Name the blood parasite species.
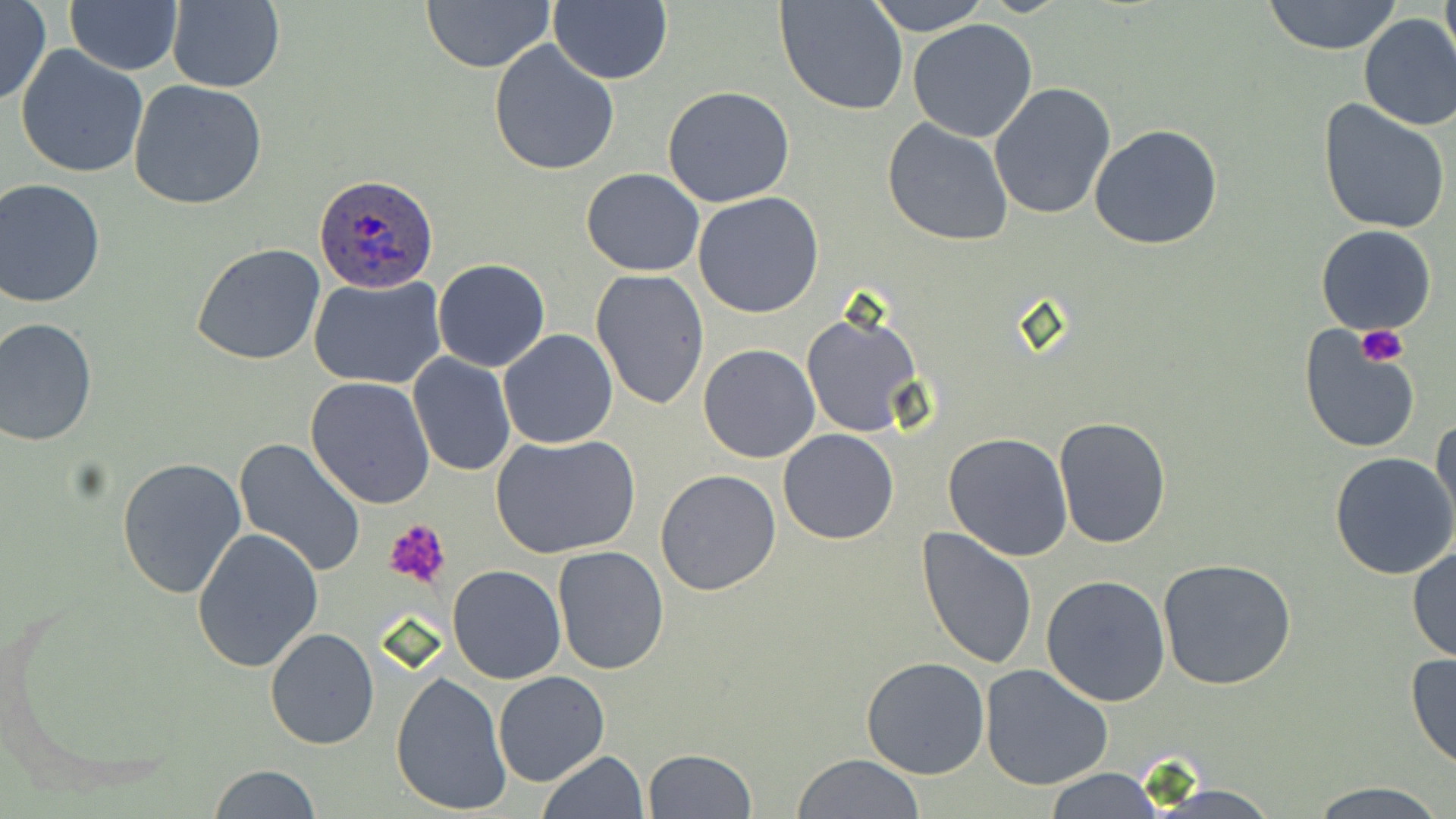

Plasmodium ovale.

Approximate bounding boxes as (x1, y1, x2, y2) in pixels. Uninfected red blood cell locations: (549, 0, 671, 84), (776, 0, 909, 117), (867, 0, 990, 35), (1263, 0, 1404, 55), (1439, 0, 1455, 71), (67, 1, 181, 75), (422, 1, 555, 73), (0, 2, 49, 106), (166, 2, 285, 92), (1357, 13, 1456, 131), (907, 18, 1039, 142), (489, 40, 620, 175), (15, 44, 149, 178), (128, 80, 268, 210), (987, 82, 1116, 220), (662, 86, 796, 209), (1317, 98, 1452, 235), (882, 118, 1014, 247), (1088, 123, 1223, 250), (581, 168, 704, 276), (0, 178, 106, 308), (692, 192, 824, 319), (1316, 224, 1438, 335), (191, 242, 327, 366), (432, 258, 550, 372), (590, 269, 710, 412), (307, 276, 447, 388), (801, 308, 924, 438), (0, 318, 97, 446), (1298, 325, 1421, 451), (497, 330, 618, 448), (699, 344, 819, 463), (407, 352, 516, 476), (305, 375, 437, 508), (1053, 417, 1171, 548), (1430, 418, 1456, 538), (777, 428, 900, 545), (942, 431, 1074, 561), (490, 432, 641, 560), (233, 439, 368, 578), (1330, 450, 1456, 579), (115, 455, 247, 600), (655, 468, 782, 595), (191, 526, 325, 673), (915, 527, 1037, 671), (1408, 545, 1456, 664), (552, 546, 670, 677), (1157, 557, 1298, 690), (444, 565, 566, 685), (1040, 573, 1171, 707), (265, 627, 380, 751), (1405, 651, 1456, 770), (862, 656, 989, 779), (979, 664, 1114, 790), (390, 671, 511, 816), (493, 671, 610, 788), (643, 748, 759, 818), (537, 750, 649, 819), (794, 752, 924, 819), (208, 764, 322, 818), (1040, 767, 1165, 819), (1303, 779, 1448, 817). Plasmodium ovale-infected red blood cell locations: (314, 175, 440, 294). Platelet locations: (1356, 326, 1407, 367), (385, 518, 453, 590). May-Grünwald-Giemsa stain. Image is 1456×819 pixels. Thin blood film. Optical microscopy. One field of a larger specimen. 1000x magnification.